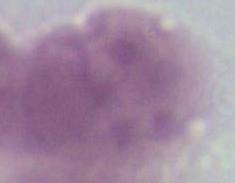

Summary:
  - Modality: micrograph
  - Magnification: 1000x
  - Identification: red blood cell